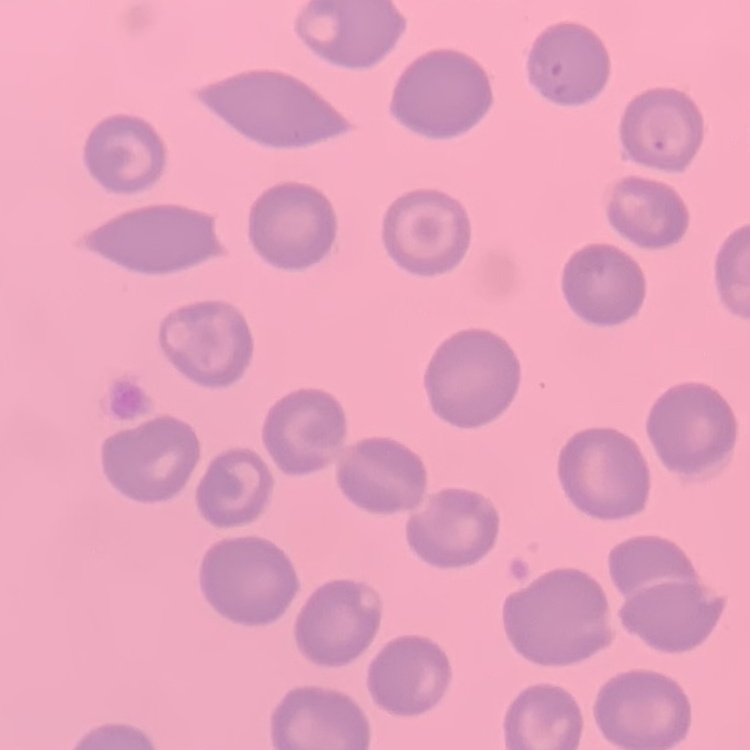

Summary:
  - Erythrocyte morphology: no rouleaux formation
  - Stain: Field's or Giemsa
  - Preparation: thin peripheral smear
  - Image type: square crop of a larger photomicrograph